Locate every Plasmodium parasite.
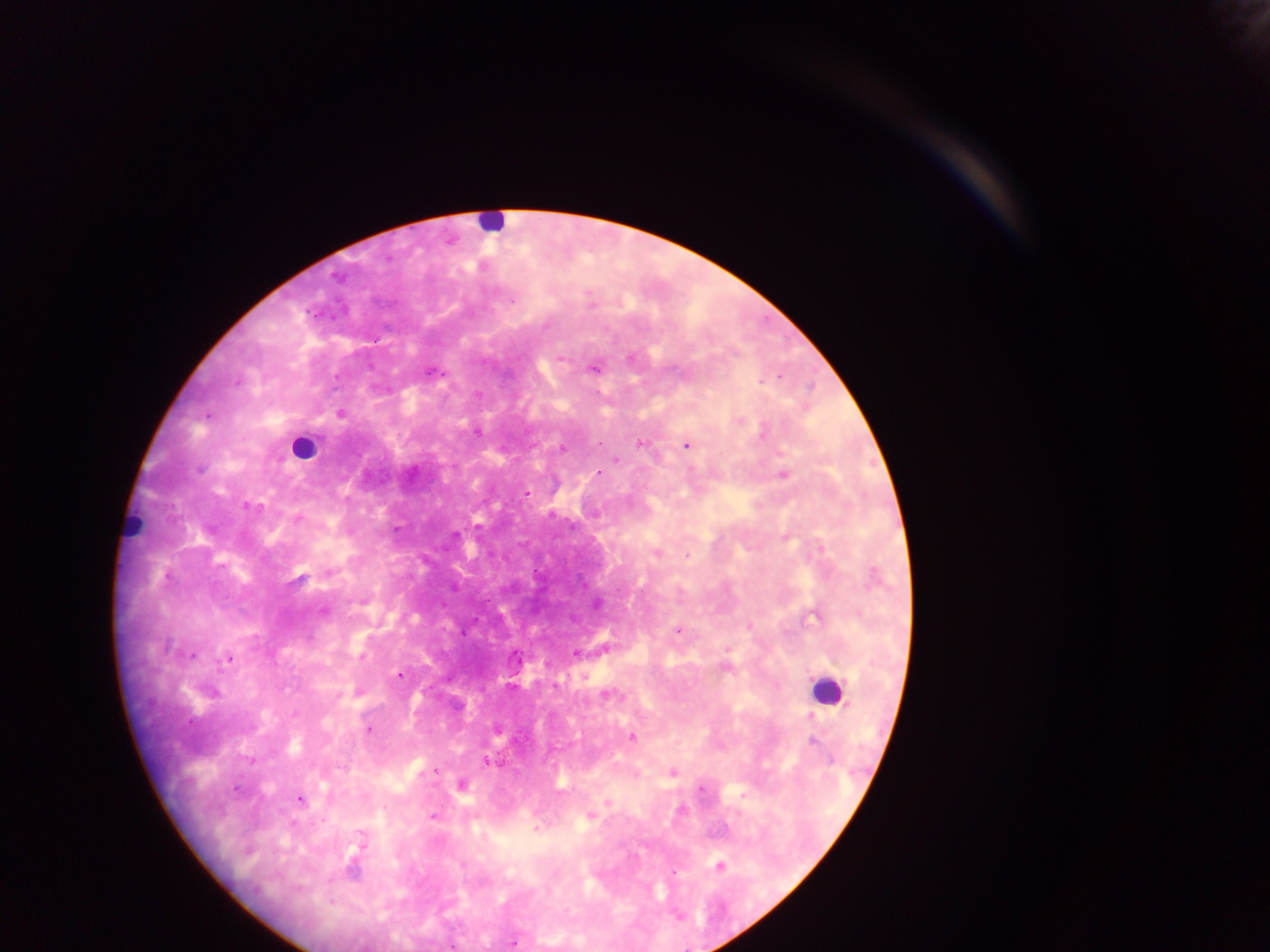
Approximate centers as x y in pixels.
Plasmodium parasites: 335 277; 512 301; 545 325; 562 358; 593 367; 430 372; 780 376; 236 382; 761 382; 340 414; 207 415; 740 421; 478 433; 639 443; 598 444; 687 445; 562 448; 616 459; 600 473; 783 474; 526 492; 248 506; 553 516; 298 519; 396 529; 455 534; 786 538; 822 548; 657 553; 687 556; 300 579; 323 610; 749 626; 678 630; 728 649; 576 654; 192 656; 229 659; 726 667; 399 675; 339 695; 607 696; 811 716; 368 730; 632 738; 813 742; 830 760; 251 761; 487 762; 436 770; 673 772; 236 789; 300 799; 608 802; 431 816; 590 816; 536 830; 360 835; 719 866; 331 903; 513 942; 451 946.

Leukocyte locations: 490 223; 303 447; 134 528; 826 690. Image is 1270×952 pixels. Sample from Ghana. Thick blood smear. Photographed through a microscope with a mobile-phone camera. One field of view.